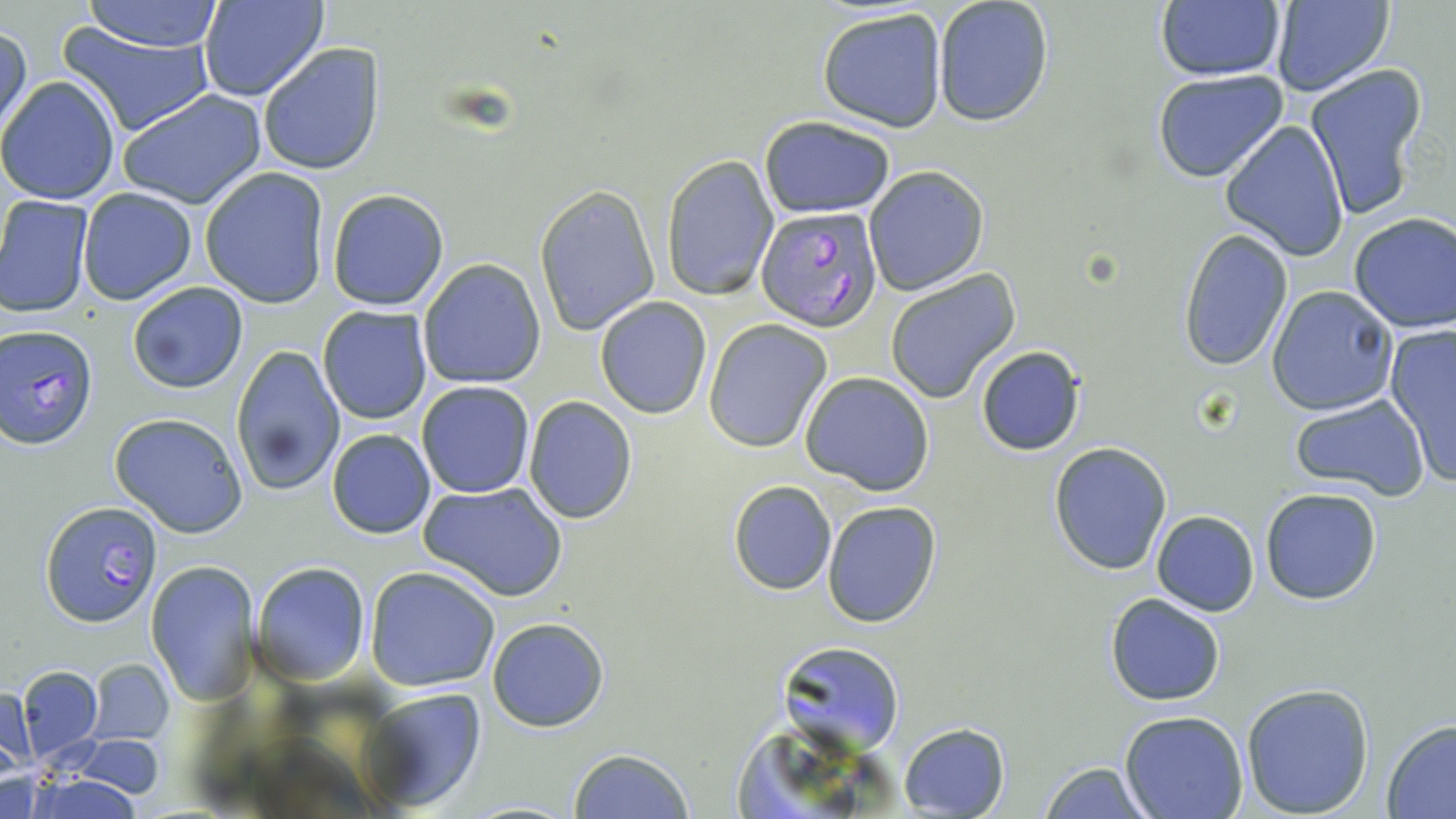

slide-level diagnosis = Plasmodium falciparum
stain = May-Grünwald-Giemsa
field of view = one of a larger specimen
uninfected red blood cell locations = approximate bounding boxes as (x1,y1)-(x2,y2) corner pairs in pixels: (76,0)-(226,51), (201,0)-(327,101), (1270,0)-(1394,96), (931,1)-(1055,126), (1153,2)-(1287,82), (817,7)-(949,131), (0,20)-(30,143), (57,21)-(219,137), (257,42)-(387,177), (1305,65)-(1427,220), (1153,70)-(1289,183), (0,75)-(122,205), (118,88)-(266,210), (758,115)-(895,218), (1219,120)-(1350,259), (662,153)-(779,301), (864,165)-(988,294), (199,167)-(331,309), (534,184)-(660,335), (77,187)-(199,307), (327,189)-(450,311), (0,195)-(95,318), (1348,211)-(1456,333), (1177,229)-(1293,371), (417,259)-(545,388), (883,269)-(1020,403), (127,280)-(249,393), (1266,286)-(1398,416), (594,296)-(712,419), (317,305)-(432,425), (704,321)-(832,452), (1384,324)-(1456,486), (229,343)-(343,496), (974,346)-(1087,457), (800,371)-(935,494), (417,381)-(536,499), (1287,393)-(1430,500), (522,397)-(638,524), (109,412)-(250,538), (327,428)-(435,538), (1049,442)-(1174,576), (420,481)-(568,603), (728,481)-(837,595), (1260,487)-(1382,604), (821,499)-(941,626), (1151,510)-(1259,616), (145,559)-(260,703), (251,561)-(371,684), (365,565)-(500,692), (1105,593)-(1225,706), (486,617)-(610,733), (784,641)-(905,754), (87,658)-(172,746), (17,666)-(103,760), (1240,681)-(1374,817), (0,686)-(35,773), (362,687)-(488,813), (1121,711)-(1248,819), (1381,720)-(1456,817), (898,722)-(1010,817), (729,729)-(859,819), (70,735)-(170,801), (568,748)-(694,819), (1039,762)-(1152,818), (17,774)-(149,818)
image size = 1456×819 pixels
preparation = thin blood smear
Plasmodium falciparum-infected red blood cell locations = approximate bounding boxes as (x1,y1)-(x2,y2) corner pairs in pixels: (755,207)-(885,331), (1,325)-(99,449), (40,499)-(162,627)
modality = optical microscopy
magnification = 1000x